Outline each Plasmodium falciparum-infected red blood cell.
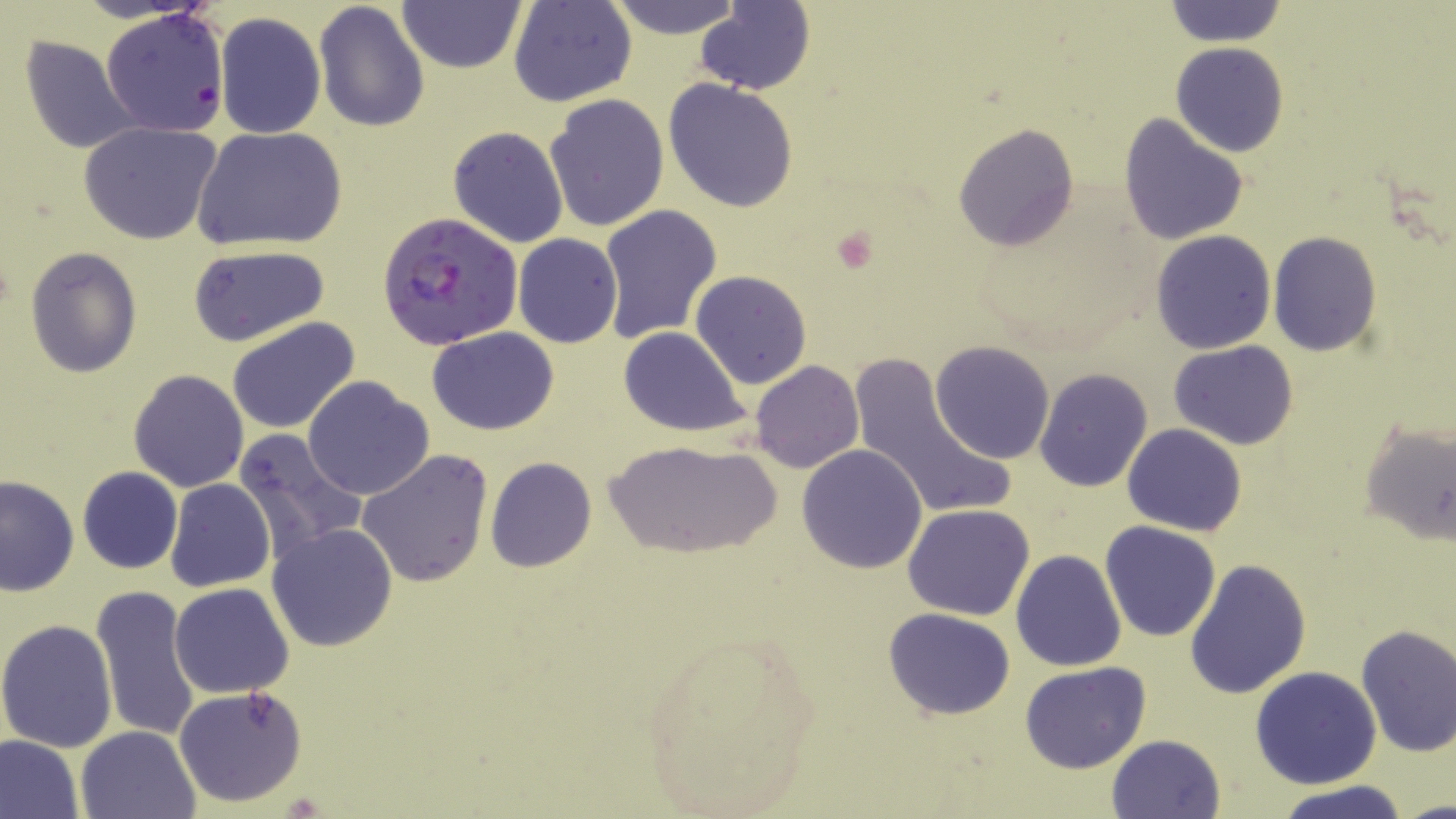

Approximate bounding boxes as (x1, y1, x2, y2) in pixels.
Plasmodium falciparum-infected red blood cells: (376, 212, 523, 350).

Uninfected red blood cell locations: (604, 0, 746, 39), (507, 1, 637, 107), (313, 2, 429, 135), (399, 2, 525, 74), (1161, 2, 1289, 47), (695, 3, 814, 94), (84, 11, 227, 138), (214, 13, 326, 139), (19, 34, 146, 156), (1171, 42, 1289, 158), (663, 79, 800, 213), (544, 93, 669, 232), (1118, 112, 1249, 247), (78, 121, 225, 246), (953, 122, 1079, 251), (447, 125, 570, 249), (191, 126, 347, 252), (598, 204, 723, 344), (1151, 230, 1277, 354), (1267, 232, 1381, 357), (513, 233, 623, 348), (187, 244, 331, 347), (25, 247, 142, 376), (691, 270, 812, 389), (227, 317, 361, 434), (428, 326, 559, 435), (617, 326, 751, 438), (929, 340, 1055, 463), (1169, 341, 1299, 451), (849, 354, 1014, 527), (751, 360, 863, 473), (1033, 368, 1154, 492), (128, 370, 249, 492), (302, 375, 434, 501), (1357, 419, 1456, 549), (1122, 422, 1247, 536), (231, 428, 366, 560), (603, 437, 783, 558), (796, 445, 929, 572), (357, 448, 493, 587), (485, 456, 597, 573), (77, 466, 182, 573), (0, 474, 79, 596), (164, 478, 276, 592), (903, 503, 1035, 620), (1100, 521, 1219, 643), (266, 522, 398, 651), (1010, 550, 1125, 671), (1183, 557, 1312, 699), (90, 583, 201, 745), (169, 583, 294, 699), (883, 607, 1016, 718), (0, 620, 119, 753), (1354, 623, 1456, 757), (634, 626, 825, 815), (1019, 661, 1150, 773), (1250, 666, 1381, 790), (174, 685, 310, 807), (76, 725, 201, 817), (1105, 733, 1226, 819), (0, 734, 84, 819), (1269, 782, 1416, 819). Platelet locations: (828, 223, 884, 276). Slide-level diagnosis: Plasmodium falciparum. Optical microscopy. Captured at 1000x magnification. Image is 1456×819 pixels. Thin blood film. One field of a larger specimen. May-Grünwald-Giemsa stain.